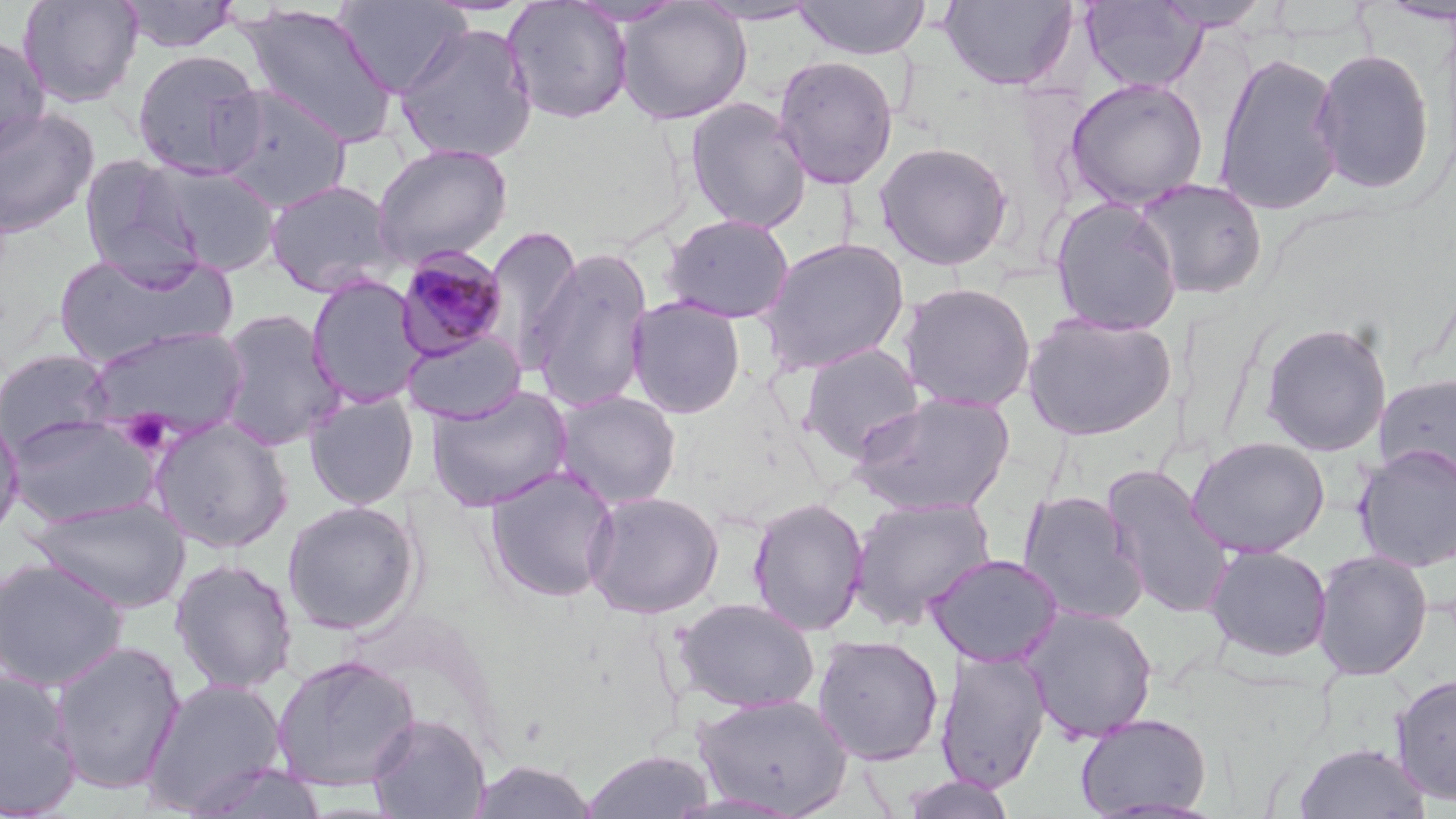

Summary:
  - Coordinate format: approximate bounding boxes as (x1, y1, x2, y2) in pixels
  - Uninfected red blood cell locations: (17, 0, 144, 107), (117, 0, 241, 53), (503, 0, 633, 124), (794, 0, 931, 60), (939, 0, 1080, 91), (1152, 0, 1272, 32), (333, 1, 468, 97), (615, 1, 752, 125), (689, 1, 825, 25), (1080, 1, 1207, 93), (238, 4, 399, 148), (395, 22, 538, 165), (0, 33, 50, 159), (1311, 47, 1437, 195), (131, 48, 266, 178), (1214, 50, 1346, 214), (773, 55, 898, 190), (1064, 76, 1209, 210), (212, 85, 352, 211), (684, 98, 812, 234), (0, 107, 99, 238), (875, 141, 1014, 271), (371, 143, 513, 267), (79, 155, 204, 279), (147, 162, 283, 275), (1132, 177, 1268, 300), (263, 178, 400, 298), (1048, 197, 1182, 335), (661, 214, 795, 324), (482, 225, 584, 372), (757, 237, 909, 375), (527, 247, 654, 413), (53, 251, 236, 367), (306, 275, 428, 409), (898, 282, 1037, 412), (626, 296, 746, 418), (214, 307, 345, 452), (1021, 311, 1178, 441), (1259, 320, 1392, 457), (84, 325, 250, 443), (401, 330, 527, 425), (796, 343, 926, 463), (0, 348, 116, 459), (1376, 372, 1456, 489), (426, 386, 573, 511), (552, 390, 682, 509), (303, 391, 420, 509), (850, 392, 1016, 517), (0, 410, 25, 544), (7, 415, 159, 528), (148, 416, 294, 554), (1186, 436, 1330, 558), (1353, 443, 1456, 573), (484, 466, 620, 603), (1102, 466, 1233, 618), (583, 490, 724, 619), (1017, 490, 1149, 625), (847, 495, 997, 630), (31, 496, 191, 612), (746, 496, 868, 637), (282, 500, 422, 635), (1204, 544, 1332, 663), (1311, 549, 1433, 681), (925, 553, 1063, 667), (0, 557, 128, 691), (170, 557, 297, 695), (675, 597, 820, 712), (1022, 606, 1159, 743), (812, 633, 944, 765), (51, 639, 186, 795), (935, 647, 1052, 792), (270, 654, 421, 792), (0, 669, 81, 817), (1390, 673, 1456, 805), (140, 677, 289, 816), (693, 692, 854, 816), (1074, 712, 1212, 817), (366, 713, 491, 819), (1292, 741, 1431, 819), (582, 749, 716, 818), (469, 759, 599, 818), (182, 760, 329, 819), (899, 773, 1017, 818)
  - Plasmodium malariae-infected red blood cell locations: (394, 246, 508, 362)
  - Platelet locations: (118, 411, 173, 456)
  - Slide-level diagnosis: Plasmodium malariae
  - Preparation: thin blood smear
  - Modality: optical microscopy
  - Stain: May-Grünwald-Giemsa
  - Image size: 1456×819 pixels
  - Field of view: one of a larger specimen
  - Magnification: 1000x